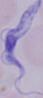
modality = photomicrograph
identification = trypanosome
magnification = 1000x